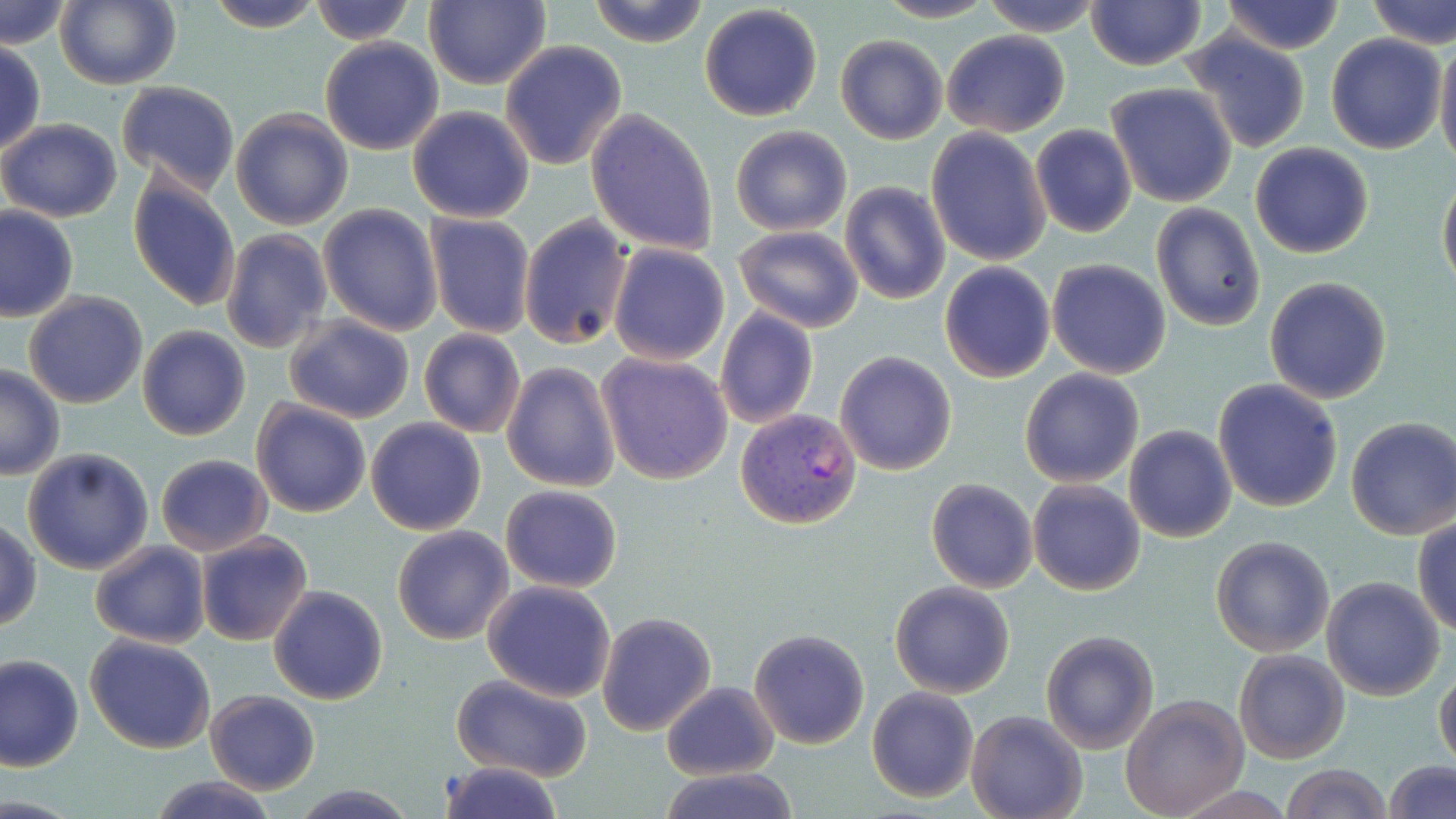
Summary:
  - Coordinate format: approximate bounding boxes as named x1/y1/x2/y2 corners in pixels
  - Uninfected red blood cell locations: (x1=56, y1=0, x2=182, y2=90), (x1=202, y1=0, x2=327, y2=33), (x1=309, y1=0, x2=416, y2=45), (x1=587, y1=0, x2=711, y2=48), (x1=872, y1=0, x2=1002, y2=23), (x1=979, y1=0, x2=1104, y2=36), (x1=1219, y1=0, x2=1347, y2=54), (x1=1365, y1=0, x2=1456, y2=50), (x1=1085, y1=1, x2=1207, y2=71), (x1=2, y1=2, x2=71, y2=49), (x1=423, y1=2, x2=552, y2=89), (x1=698, y1=4, x2=823, y2=121), (x1=940, y1=31, x2=1070, y2=137), (x1=1179, y1=32, x2=1311, y2=154), (x1=835, y1=34, x2=948, y2=145), (x1=1325, y1=34, x2=1447, y2=153), (x1=1435, y1=34, x2=1456, y2=173), (x1=319, y1=37, x2=444, y2=154), (x1=0, y1=40, x2=46, y2=159), (x1=500, y1=40, x2=629, y2=171), (x1=116, y1=81, x2=240, y2=194), (x1=1106, y1=82, x2=1237, y2=208), (x1=407, y1=106, x2=536, y2=223), (x1=585, y1=108, x2=719, y2=255), (x1=230, y1=109, x2=354, y2=230), (x1=0, y1=118, x2=123, y2=221), (x1=1029, y1=124, x2=1137, y2=238), (x1=730, y1=125, x2=851, y2=236), (x1=926, y1=128, x2=1052, y2=267), (x1=1249, y1=143, x2=1375, y2=258), (x1=1438, y1=173, x2=1456, y2=293), (x1=126, y1=174, x2=242, y2=313), (x1=839, y1=180, x2=950, y2=305), (x1=1150, y1=202, x2=1266, y2=331), (x1=318, y1=204, x2=443, y2=335), (x1=0, y1=206, x2=78, y2=322), (x1=424, y1=213, x2=536, y2=339), (x1=519, y1=214, x2=633, y2=350), (x1=732, y1=224, x2=865, y2=333), (x1=220, y1=229, x2=333, y2=354), (x1=609, y1=243, x2=729, y2=365), (x1=1047, y1=258, x2=1171, y2=380), (x1=938, y1=262, x2=1055, y2=382), (x1=1264, y1=277, x2=1393, y2=403), (x1=22, y1=291, x2=148, y2=409), (x1=715, y1=305, x2=819, y2=428), (x1=283, y1=314, x2=415, y2=423), (x1=138, y1=325, x2=250, y2=440), (x1=418, y1=328, x2=526, y2=438), (x1=835, y1=350, x2=957, y2=475), (x1=597, y1=352, x2=732, y2=484), (x1=502, y1=362, x2=620, y2=493), (x1=0, y1=364, x2=65, y2=480), (x1=1019, y1=367, x2=1145, y2=487), (x1=1211, y1=377, x2=1343, y2=512), (x1=250, y1=398, x2=374, y2=517), (x1=366, y1=416, x2=487, y2=535), (x1=1344, y1=418, x2=1456, y2=539), (x1=1123, y1=424, x2=1236, y2=542), (x1=22, y1=447, x2=155, y2=574), (x1=155, y1=453, x2=271, y2=555), (x1=926, y1=478, x2=1038, y2=593), (x1=1027, y1=480, x2=1145, y2=596), (x1=501, y1=485, x2=622, y2=593), (x1=1412, y1=514, x2=1456, y2=636), (x1=1, y1=519, x2=41, y2=633), (x1=391, y1=525, x2=513, y2=645), (x1=195, y1=531, x2=313, y2=646), (x1=1210, y1=535, x2=1336, y2=657), (x1=90, y1=541, x2=210, y2=649), (x1=1321, y1=577, x2=1445, y2=700), (x1=483, y1=580, x2=617, y2=702), (x1=890, y1=581, x2=1016, y2=698), (x1=268, y1=585, x2=388, y2=705), (x1=595, y1=611, x2=717, y2=736), (x1=748, y1=628, x2=870, y2=749), (x1=1041, y1=630, x2=1158, y2=753), (x1=84, y1=634, x2=216, y2=754), (x1=1233, y1=648, x2=1351, y2=763), (x1=1, y1=654, x2=83, y2=771), (x1=1435, y1=669, x2=1456, y2=769), (x1=450, y1=675, x2=592, y2=781), (x1=661, y1=681, x2=778, y2=781), (x1=867, y1=687, x2=979, y2=802), (x1=206, y1=690, x2=320, y2=794), (x1=1120, y1=695, x2=1249, y2=818), (x1=966, y1=708, x2=1088, y2=819), (x1=1382, y1=759, x2=1456, y2=819), (x1=436, y1=760, x2=566, y2=819), (x1=1278, y1=763, x2=1392, y2=819), (x1=659, y1=768, x2=800, y2=819), (x1=145, y1=775, x2=277, y2=818), (x1=290, y1=784, x2=416, y2=818)
  - Plasmodium vivax-infected red blood cell locations: (x1=734, y1=409, x2=862, y2=531)
  - Slide-level diagnosis: Plasmodium vivax
  - Preparation: thin blood film
  - Stain: May-Grünwald-Giemsa
  - Field of view: one of a larger specimen
  - Magnification: 1000x
  - Image size: 1456×819 pixels
  - Modality: optical microscopy